Identify the parasite.
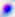

Toxoplasma gondii.

Photomicrograph. 400x magnification.